Find each parasitized RBC.
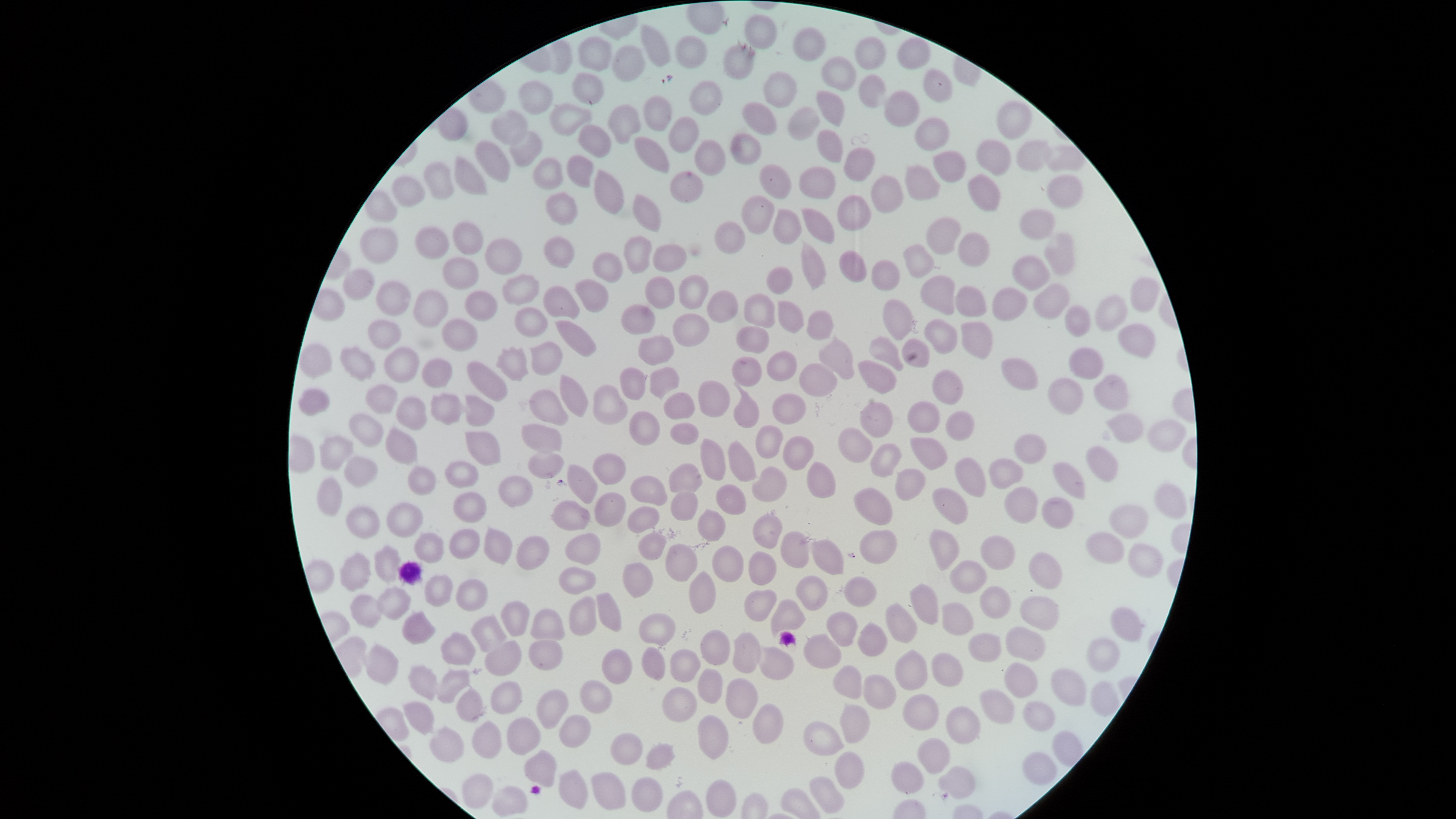
No parasitized RBCs identified.

Approximate bounding boxes as {left, top, right, bottom} in pixels. Uninfected RBCs: {744, 14, 778, 49}, {641, 24, 671, 67}, {793, 27, 827, 61}, {675, 35, 708, 69}, {576, 36, 612, 72}, {854, 36, 886, 70}, {897, 37, 931, 70}, {722, 44, 755, 80}, {612, 45, 645, 82}, {821, 56, 857, 91}, {923, 68, 952, 102}, {571, 71, 605, 105}, {763, 71, 798, 108}, {857, 74, 886, 108}, {518, 80, 553, 115}, {689, 80, 723, 116}, {816, 90, 845, 126}, {884, 90, 920, 128}, {643, 95, 672, 132}, {996, 100, 1032, 140}, {742, 101, 777, 135}, {548, 103, 592, 136}, {607, 104, 641, 145}, {787, 106, 820, 141}, {490, 110, 528, 145}, {668, 115, 700, 153}, {915, 117, 950, 151}, {578, 124, 612, 159}, {816, 128, 844, 163}, {509, 131, 542, 167}, {730, 133, 762, 165}, {633, 136, 670, 173}, {694, 139, 726, 176}, {976, 139, 1012, 176}, {474, 140, 511, 183}, {1015, 140, 1051, 172}, {1044, 144, 1086, 172}, {843, 147, 876, 182}, {932, 151, 966, 183}, {566, 154, 593, 188}, {454, 156, 487, 195}, {532, 157, 564, 191}, {423, 161, 454, 200}, {759, 164, 792, 199}, {904, 164, 941, 201}, {798, 166, 837, 200}, {594, 169, 625, 214}, {669, 171, 704, 203}, {966, 174, 1001, 212}, {391, 175, 426, 207}, {870, 175, 904, 214}, {1046, 175, 1084, 208}, {364, 190, 397, 222}, {545, 191, 578, 225}, {632, 194, 662, 233}, {836, 194, 872, 231}, {741, 195, 775, 235}, {800, 207, 835, 244}, {772, 208, 802, 244}, {1018, 208, 1056, 240}, {926, 216, 962, 255}, {452, 221, 484, 256}, {714, 221, 745, 254}, {359, 225, 398, 264}, {414, 226, 450, 260}, {957, 232, 990, 267}, {1044, 233, 1075, 276}, {623, 235, 652, 274}, {543, 236, 574, 269}, {485, 238, 522, 274}, {801, 240, 827, 291}, {652, 243, 687, 273}, {902, 244, 935, 278}, {837, 250, 867, 283}, {592, 252, 623, 283}, {1011, 255, 1050, 291}, {441, 257, 479, 290}, {871, 259, 900, 292}, {766, 266, 793, 295}, {342, 268, 375, 300}, {502, 273, 540, 305}, {678, 274, 709, 310}, {919, 275, 955, 315}, {644, 276, 675, 310}, {1130, 277, 1160, 312}, {574, 279, 609, 313}, {375, 280, 411, 317}, {1032, 283, 1069, 319}, {543, 286, 580, 319}, {954, 286, 987, 317}, {991, 287, 1028, 322}, {412, 289, 449, 328}, {464, 290, 498, 321}, {706, 290, 739, 323}, {743, 293, 776, 328}, {1094, 295, 1128, 331}, {882, 299, 913, 340}, {777, 300, 804, 333}, {620, 304, 656, 335}, {1064, 304, 1091, 337}, {514, 306, 547, 338}, {806, 310, 834, 341}, {672, 313, 710, 347}, {440, 318, 478, 352}, {924, 318, 958, 354}, {366, 319, 402, 349}, {554, 320, 597, 357}, {960, 321, 993, 360}, {1117, 323, 1156, 358}, {735, 326, 770, 353}, {638, 334, 675, 366}, {818, 334, 855, 380}, {869, 335, 903, 371}, {901, 338, 930, 368}, {528, 341, 563, 375}, {299, 343, 332, 377}, {339, 346, 377, 382}, {383, 346, 419, 383}, {495, 347, 529, 382}, {1068, 347, 1104, 380}, {766, 350, 797, 382}, {732, 356, 762, 387}, {421, 357, 453, 389}, {1001, 357, 1038, 390}, {466, 360, 508, 402}, {857, 360, 898, 394}, {798, 363, 838, 397}, {649, 366, 680, 400}, {619, 367, 646, 400}, {932, 368, 964, 406}, {559, 374, 589, 417}, {1094, 374, 1130, 410}, {1048, 378, 1083, 415}, {697, 380, 730, 417}, {733, 381, 759, 428}, {364, 384, 398, 414}, {592, 384, 628, 425}, {297, 388, 330, 417}, {528, 389, 569, 426}, {663, 391, 695, 420}, {430, 393, 470, 425}, {772, 393, 807, 424}, {464, 395, 495, 427}, {395, 396, 427, 431}, {907, 400, 940, 433}, {859, 402, 894, 437}, {628, 410, 660, 446}, {945, 410, 975, 441}, {348, 413, 384, 447}, {1106, 413, 1144, 443}, {1147, 419, 1188, 451}, {670, 422, 699, 445}, {521, 424, 562, 453}, {755, 424, 784, 459}, {385, 426, 418, 465}, {837, 427, 873, 463}, {464, 431, 501, 466}, {1012, 433, 1047, 464}, {319, 434, 354, 471}, {782, 435, 815, 471}, {909, 437, 948, 471}, {700, 438, 727, 481}, {728, 440, 758, 482}, {869, 442, 902, 478}, {1085, 446, 1118, 483}, {528, 452, 564, 479}, {592, 453, 626, 485}, {343, 456, 378, 488}, {954, 457, 987, 498}, {989, 458, 1024, 490}, {444, 461, 479, 488}, {806, 461, 836, 498}, {1052, 462, 1086, 500}, {668, 463, 703, 493}, {566, 464, 598, 504}, {407, 465, 437, 495}, {751, 465, 788, 502}, {894, 468, 926, 501}, {497, 475, 533, 508}, {630, 475, 667, 506}, {315, 476, 342, 516}, {1153, 482, 1187, 519}, {716, 484, 747, 515}, {1004, 486, 1038, 525}, {853, 487, 893, 526}, {932, 487, 968, 525}, {670, 490, 699, 521}, {453, 491, 487, 523}, {593, 492, 626, 527}, {1041, 496, 1075, 529}, {550, 500, 591, 531}, {385, 502, 424, 538}, {1109, 504, 1148, 539}, {344, 505, 380, 538}, {627, 506, 661, 534}, {697, 508, 726, 541}, {752, 512, 783, 549}, {483, 527, 513, 565}, {448, 528, 480, 560}, {859, 529, 898, 565}, {929, 529, 960, 571}, {780, 531, 810, 568}, {414, 532, 444, 564}, {638, 532, 667, 560}, {1085, 532, 1125, 564}, {565, 533, 601, 565}, {981, 534, 1016, 569}, {516, 535, 550, 571}, {810, 539, 844, 575}, {665, 543, 698, 582}, {1127, 543, 1163, 578}, {373, 545, 401, 582}, {711, 545, 744, 582}, {339, 551, 372, 592}, {748, 551, 777, 585}, {1029, 551, 1062, 590}, {949, 560, 988, 593}, {622, 562, 653, 598}, {558, 566, 597, 595}, {688, 570, 717, 614}, {423, 574, 453, 607}, {795, 575, 829, 610}, {842, 576, 877, 607}, {456, 578, 488, 611}, {910, 583, 939, 624}, {376, 586, 412, 620}, {980, 586, 1011, 619}, {743, 589, 777, 621}, {595, 592, 622, 632}, {350, 593, 384, 629}, {568, 596, 596, 636}, {1019, 596, 1060, 630}, {770, 599, 806, 637}, {500, 600, 530, 637}, {942, 601, 974, 636}, {885, 602, 918, 643}, {1110, 606, 1143, 642}, {530, 609, 565, 641}, {401, 611, 436, 645}, {825, 611, 858, 647}, {638, 613, 676, 646}, {470, 614, 506, 652}, {857, 622, 888, 657}, {1005, 625, 1047, 661}, {699, 629, 730, 665}, {441, 632, 476, 666}, {732, 632, 761, 674}, {968, 632, 1002, 663}, {803, 633, 842, 669}, {1086, 637, 1120, 672}, {484, 640, 522, 676}, {528, 640, 564, 671}, {365, 643, 399, 686}, {641, 646, 666, 681}, {758, 646, 795, 680}, {601, 648, 632, 685}, {669, 649, 701, 683}, {894, 649, 928, 690}, {930, 652, 964, 688}, {1003, 662, 1038, 698}, {407, 664, 439, 700}, {832, 664, 862, 699}, {437, 668, 471, 703}, {697, 668, 723, 704}, {1050, 668, 1086, 706}, {862, 674, 897, 710}, {725, 677, 758, 719}, {580, 680, 613, 714}, {1089, 680, 1121, 717}, {490, 681, 522, 715}, {456, 686, 484, 723}, {662, 687, 697, 722}, {536, 689, 569, 729}, {979, 689, 1015, 725}, {902, 694, 940, 731}, {402, 700, 435, 735}, {1023, 700, 1056, 732}, {752, 703, 784, 744}, {840, 703, 870, 743}, {946, 706, 981, 744}, {558, 714, 591, 748}, {697, 714, 729, 759}, {506, 717, 541, 755}, {802, 720, 844, 756}, {471, 721, 503, 759}, {429, 725, 464, 763}, {610, 732, 643, 766}, {916, 738, 950, 775}, {645, 743, 676, 770}, {523, 749, 558, 788}, {834, 751, 866, 789}, {1022, 752, 1056, 785}, {890, 761, 925, 795}, {937, 766, 976, 799}, {557, 769, 589, 809}, {590, 772, 626, 811}, {461, 773, 494, 809}, {809, 776, 844, 814}, {631, 777, 664, 813}, {706, 779, 737, 818}, {491, 785, 528, 817}. Image is 1456×819 pixels. The visible region is circular. Smartphone photograph through the microscope eyepiece. Giemsa-stained preparation. Thin blood smear. Single field of view.